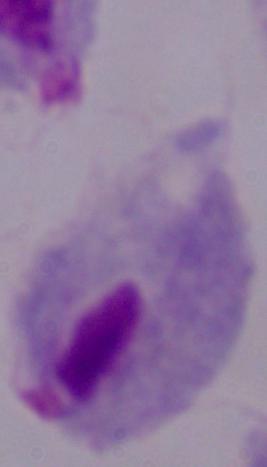 A trichomonad is seen. Photomicrograph. 1000x magnification.